Identify the parasite.
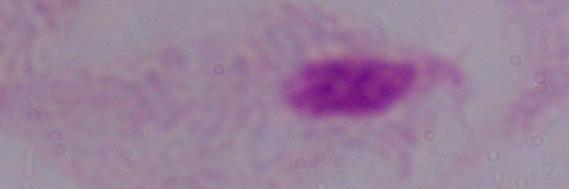

This is a trichomonad.

1000x magnification. Photomicrograph.